Report the malaria status of this cell.
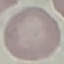
It is uninfected.

image_type: cell patch, automatically extracted from a larger field of view and resized to 64 × 64 pixels
stain: Giemsa
preparation: thin blood film
capture: smartphone through the microscope eyepiece